Identify the blood parasite species.
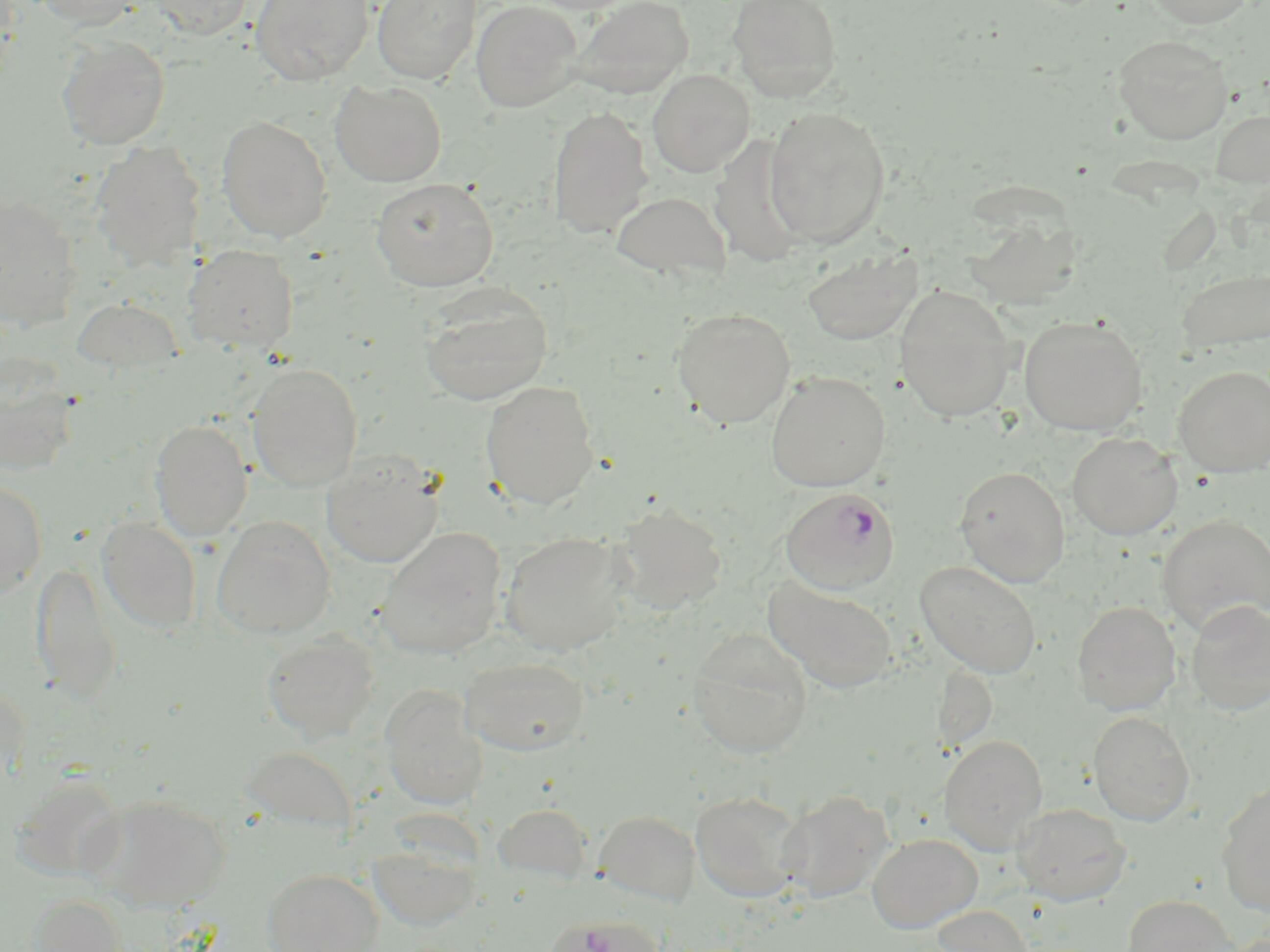
Plasmodium falciparum.

Summary:
  - Coordinate format: approximate bounding boxes as [x1, y1, x2, y2] in pixels
  - Uninfected red blood cell locations: [30, 0, 144, 29], [146, 0, 255, 39], [251, 0, 374, 85], [371, 0, 481, 84], [471, 0, 583, 112], [569, 0, 694, 99], [727, 0, 843, 101], [1143, 0, 1256, 28], [1113, 34, 1233, 144], [57, 35, 170, 150], [647, 69, 754, 177], [330, 80, 447, 187], [548, 105, 652, 238], [763, 105, 891, 249], [1210, 109, 1270, 188], [216, 114, 332, 242], [90, 141, 206, 271], [371, 177, 499, 291], [611, 190, 732, 282], [0, 194, 83, 332], [960, 209, 1084, 310], [183, 245, 299, 354], [802, 246, 923, 344], [1176, 268, 1270, 353], [894, 286, 1018, 423], [418, 287, 554, 406], [70, 297, 185, 376], [671, 307, 796, 428], [1019, 316, 1147, 436], [0, 357, 80, 477], [247, 363, 363, 491], [1173, 365, 1270, 476], [765, 371, 891, 492], [480, 380, 599, 509], [150, 419, 253, 541], [1067, 432, 1183, 539], [322, 450, 444, 568], [954, 465, 1070, 587], [0, 480, 48, 598], [612, 503, 728, 613], [1157, 514, 1270, 635], [96, 517, 201, 635], [212, 517, 335, 639], [376, 527, 507, 660], [499, 532, 632, 655], [31, 560, 123, 706], [915, 560, 1042, 678], [764, 578, 899, 694], [1185, 599, 1270, 716], [1072, 600, 1181, 716], [687, 629, 813, 758], [262, 632, 379, 743], [459, 656, 589, 756], [0, 683, 29, 786], [380, 685, 488, 810], [1088, 711, 1195, 826], [940, 735, 1048, 855], [240, 745, 359, 836], [12, 774, 127, 883], [1216, 783, 1270, 917], [777, 789, 894, 904], [690, 791, 806, 902], [88, 793, 231, 912], [1012, 802, 1131, 905], [494, 803, 594, 885], [595, 810, 701, 907], [867, 833, 982, 933], [368, 843, 483, 932], [262, 868, 383, 952], [28, 893, 127, 952], [1122, 895, 1236, 952], [930, 904, 1033, 952], [546, 915, 664, 952]
  - Plasmodium falciparum-infected red blood cell locations: [781, 487, 900, 595]
  - Magnification: 1000x
  - Preparation: thin blood smear
  - Modality: optical microscopy
  - Image size: 1270×952 pixels
  - Stain: May-Grünwald-Giemsa
  - Field of view: one of a larger specimen